Classify this cell by malaria status.
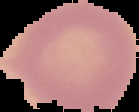
Uninfected.

The area outside the segmented cell region is set to black. Image is 139×112 pixels. From a thin blood smear.